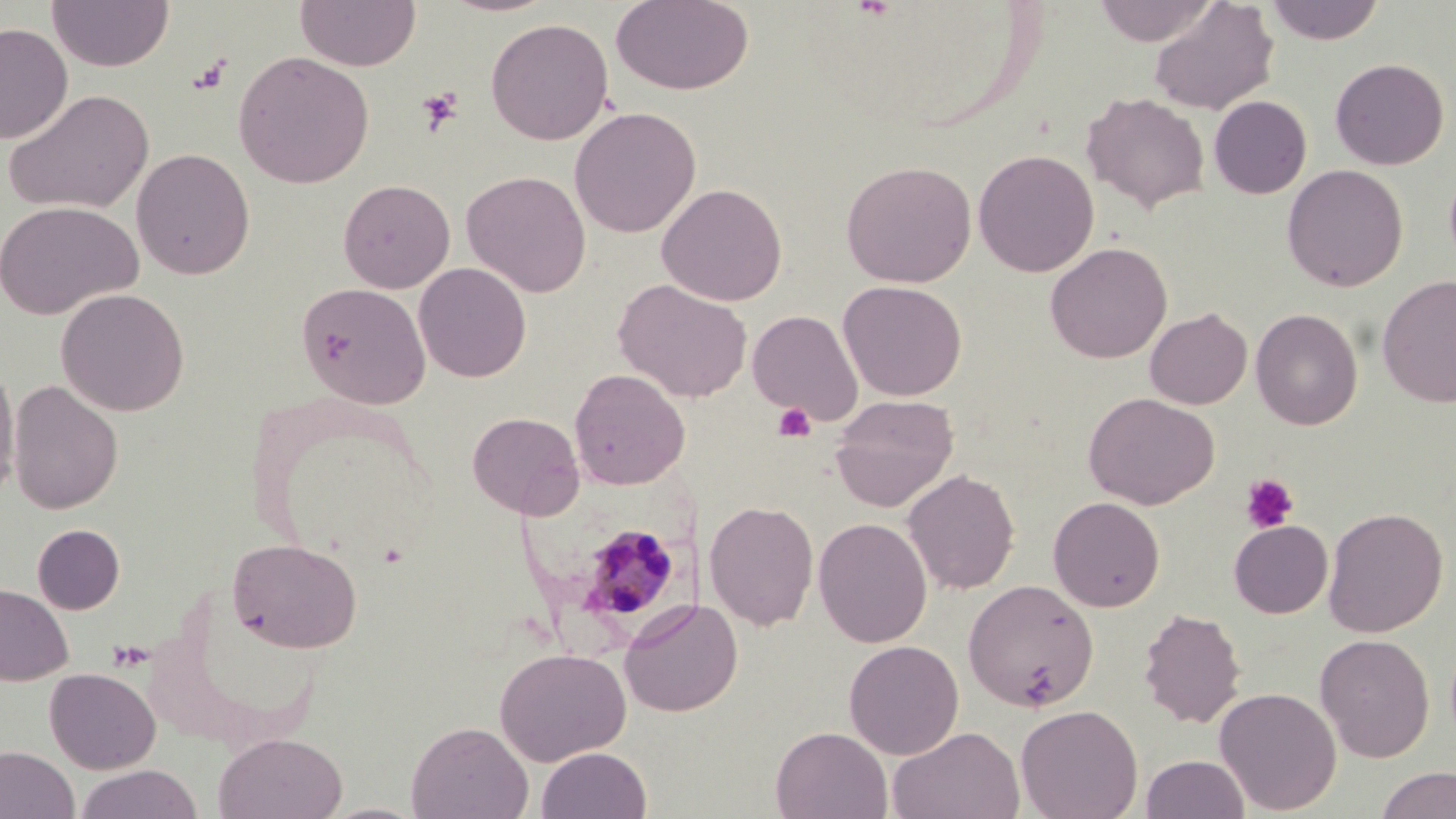
slide-level diagnosis = Plasmodium malariae
uninfected red blood cell locations = approximate bounding boxes as [x1, y1, x2, y2] in pixels: [47, 0, 174, 72], [294, 0, 421, 72], [437, 0, 561, 17], [610, 0, 755, 96], [1092, 0, 1220, 46], [1265, 0, 1385, 45], [1148, 1, 1279, 115], [485, 17, 614, 145], [0, 22, 73, 143], [233, 50, 374, 188], [1330, 57, 1449, 170], [3, 88, 154, 215], [1081, 92, 1210, 213], [1209, 96, 1312, 199], [568, 106, 702, 238], [131, 148, 255, 279], [973, 149, 1099, 277], [840, 160, 977, 288], [1282, 164, 1408, 292], [462, 170, 591, 297], [337, 179, 455, 293], [657, 182, 788, 306], [0, 201, 142, 320], [1045, 241, 1172, 363], [413, 262, 532, 382], [1377, 274, 1456, 408], [614, 279, 752, 402], [838, 280, 967, 401], [296, 281, 431, 409], [55, 288, 190, 416], [1145, 307, 1252, 409], [1250, 308, 1363, 430], [747, 309, 863, 425], [0, 364, 20, 501], [569, 369, 690, 489], [8, 380, 123, 514], [1083, 392, 1220, 509], [830, 395, 959, 512], [467, 411, 584, 519], [902, 469, 1020, 594], [1047, 496, 1165, 612], [703, 499, 819, 631], [1323, 506, 1448, 637], [813, 517, 932, 648], [1229, 520, 1333, 618], [32, 524, 125, 614], [227, 537, 363, 653], [963, 579, 1099, 712], [0, 583, 74, 686], [619, 598, 743, 718], [1137, 608, 1246, 728], [1315, 633, 1435, 762], [843, 640, 964, 759], [494, 647, 631, 766], [45, 668, 161, 774], [1214, 687, 1342, 815], [1015, 704, 1143, 819], [406, 721, 533, 819], [887, 725, 1025, 819], [771, 726, 893, 818], [213, 732, 347, 819], [0, 745, 79, 819], [536, 746, 652, 819], [1142, 755, 1249, 819], [74, 764, 203, 819], [1376, 766, 1456, 819], [317, 802, 429, 819]
Plasmodium malariae-infected red blood cell locations = approximate bounding boxes as [x1, y1, x2, y2] in pixels: [569, 521, 688, 632]
image size = 1456×819 pixels
magnification = 1000x
field of view = single
modality = optical microscopy
platelet locations = approximate bounding boxes as [x1, y1, x2, y2] in pixels: [188, 56, 232, 95], [416, 88, 463, 135], [772, 402, 817, 442], [1240, 474, 1299, 533]
stain = May-Grünwald-Giemsa
preparation = thin blood smear